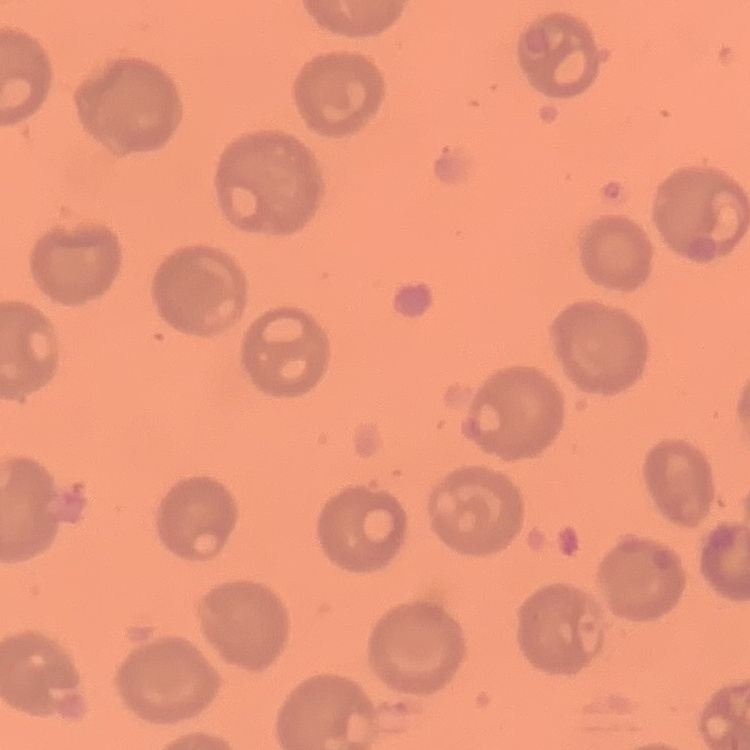

red blood cell morphology = no rouleaux formation
preparation = thin blood film
image type = square crop of a larger photomicrograph
stain = Field's or Giemsa